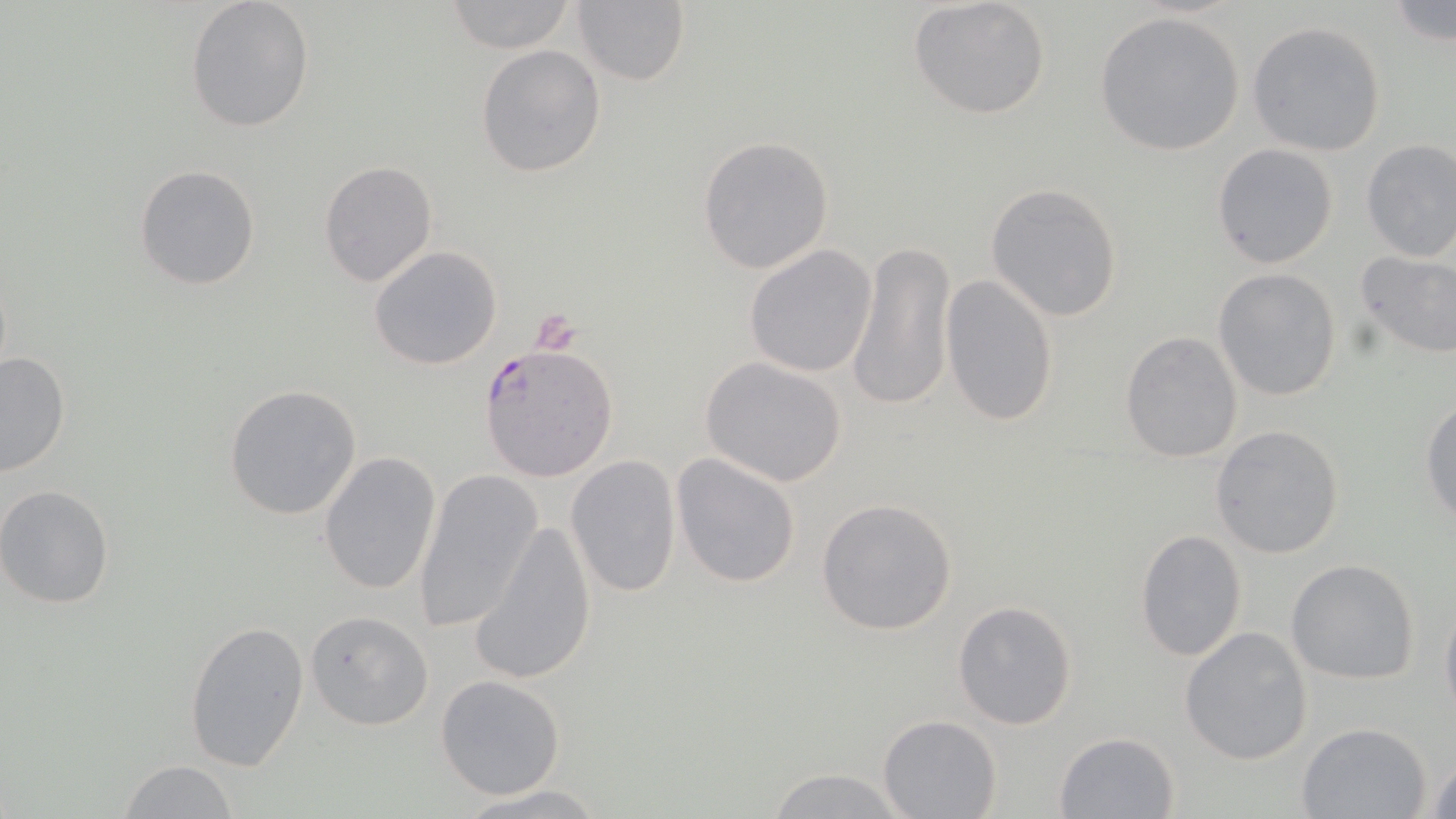
slide-level diagnosis = Plasmodium falciparum
magnification = 1000x
Plasmodium falciparum-infected red blood cell locations = approximate bounding boxes as [x1, y1, x2, y2] in pixels: [479, 343, 617, 483]
field of view = single
platelet locations = approximate bounding boxes as [x1, y1, x2, y2] in pixels: [531, 311, 581, 353]
image size = 1456×819 pixels
stain = May-Grünwald-Giemsa
preparation = thin blood film
modality = light microscopy
uninfected red blood cell locations = approximate bounding boxes as [x1, y1, x2, y2] in pixels: [185, 0, 315, 133], [908, 0, 1051, 120], [439, 1, 579, 53], [1385, 1, 1456, 50], [571, 2, 690, 86], [1094, 11, 1248, 157], [1248, 21, 1387, 157], [475, 45, 606, 179], [697, 135, 835, 274], [1359, 139, 1456, 262], [1211, 144, 1339, 268], [318, 162, 438, 287], [135, 165, 260, 289], [986, 184, 1126, 323], [846, 240, 955, 414], [369, 245, 503, 371], [743, 245, 877, 377], [1354, 247, 1456, 359], [1213, 268, 1343, 401], [940, 273, 1058, 428], [1119, 331, 1242, 463], [0, 351, 71, 478], [700, 356, 848, 487], [224, 384, 364, 521], [1420, 394, 1456, 530], [1211, 425, 1345, 559], [319, 451, 442, 595], [670, 452, 802, 590], [565, 455, 682, 599], [412, 468, 543, 633], [0, 485, 118, 608], [815, 497, 958, 635], [470, 517, 597, 685], [1135, 529, 1248, 663], [1287, 559, 1420, 684], [951, 599, 1078, 730], [1441, 602, 1456, 723], [305, 610, 434, 731], [183, 618, 309, 772], [1179, 626, 1314, 766], [435, 674, 565, 799], [877, 714, 1002, 818], [1295, 722, 1432, 818], [1053, 731, 1180, 817], [1426, 753, 1456, 817], [117, 760, 238, 819], [763, 767, 912, 819], [454, 783, 612, 818]